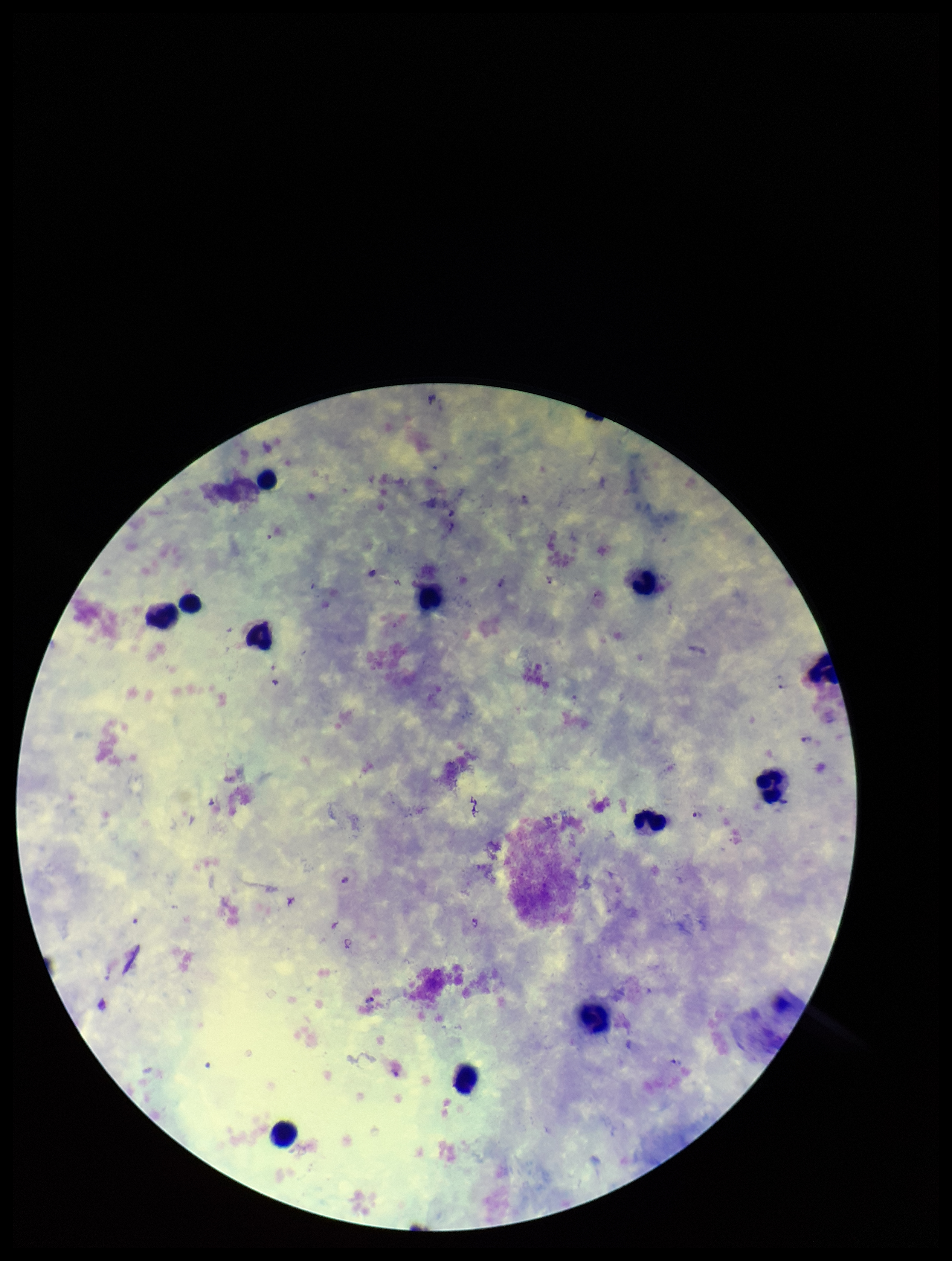 Stained with Giemsa. Species reported for this patient: Plasmodium vivax. Photographed through the microscope eyepiece with a smartphone camera. Parasite count: 7. Single field of view. Plasmodium parasites: seen. Leukocyte count: 11. Image is 952×1261 pixels. Preparation: thick smear. Patient malaria status: positive.